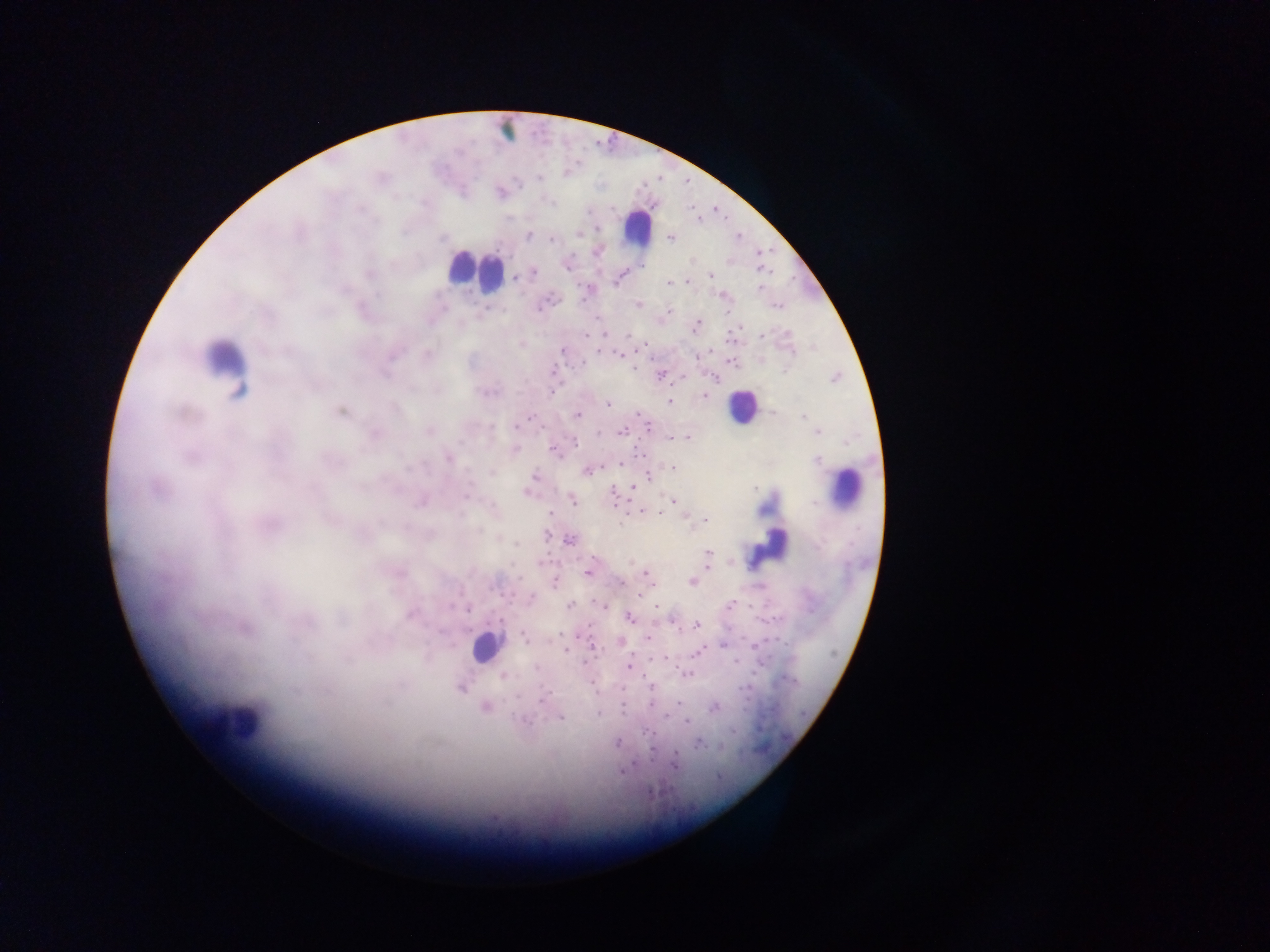
capture = mobile-phone photograph through a microscope
image size = 1270×952 pixels
malaria parasite locations = approximate centers as {x, y} in pixels: {538, 178}, {500, 193}, {577, 232}, {526, 235}, {670, 237}, {552, 240}, {597, 250}, {566, 264}, {534, 272}, {710, 274}, {618, 276}, {515, 278}, {687, 281}, {669, 282}, {758, 289}, {588, 291}, {549, 299}, {638, 304}, {777, 305}, {667, 312}, {697, 324}, {761, 334}, {584, 336}, {629, 336}, {520, 344}, {563, 349}, {600, 351}, {618, 353}, {426, 355}, {731, 361}, {632, 368}, {661, 374}, {836, 377}, {489, 391}, {551, 391}, {703, 395}, {669, 402}, {607, 405}, {341, 411}, {639, 414}, {577, 415}, {531, 416}, {804, 417}, {648, 427}, {429, 430}, {622, 430}, {818, 432}, {373, 434}, {687, 438}, {574, 440}, {516, 449}, {556, 451}, {640, 453}, {448, 458}, {620, 462}, {672, 467}, {587, 469}, {535, 476}, {632, 487}, {528, 491}, {614, 491}, {465, 494}, {423, 500}, {571, 500}, {672, 501}, {641, 512}, {658, 512}, {551, 513}, {704, 521}, {268, 524}, {569, 540}, {517, 543}, {708, 552}, {708, 566}, {587, 572}, {647, 576}, {692, 581}, {554, 582}, {622, 582}, {639, 596}, {529, 598}, {603, 604}, {568, 606}, {655, 606}, {410, 612}, {629, 617}, {697, 625}, {244, 627}, {523, 635}, {647, 637}, {619, 641}, {723, 644}, {591, 645}, {696, 653}, {664, 657}, {628, 666}, {537, 669}, {686, 673}, {503, 676}, {652, 685}, {461, 687}, {542, 699}, {651, 703}, {677, 703}, {485, 707}, {714, 707}, {560, 717}, {687, 720}, {617, 742}, {698, 744}, {674, 762}, {622, 771}
field of view = single
leukocyte locations = approximate centers as {x, y} in pixels: {507, 129}, {637, 226}, {474, 270}, {222, 367}, {741, 406}, {845, 487}, {769, 546}, {486, 646}, {236, 723}
country = Ghana
preparation = thick blood smear